Name the parasite shown.
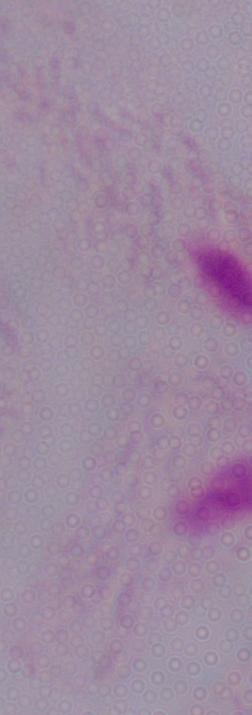
This is a trichomonad.

Captured at 1000x magnification. Micrograph.